Locate and identify every blood parasite.
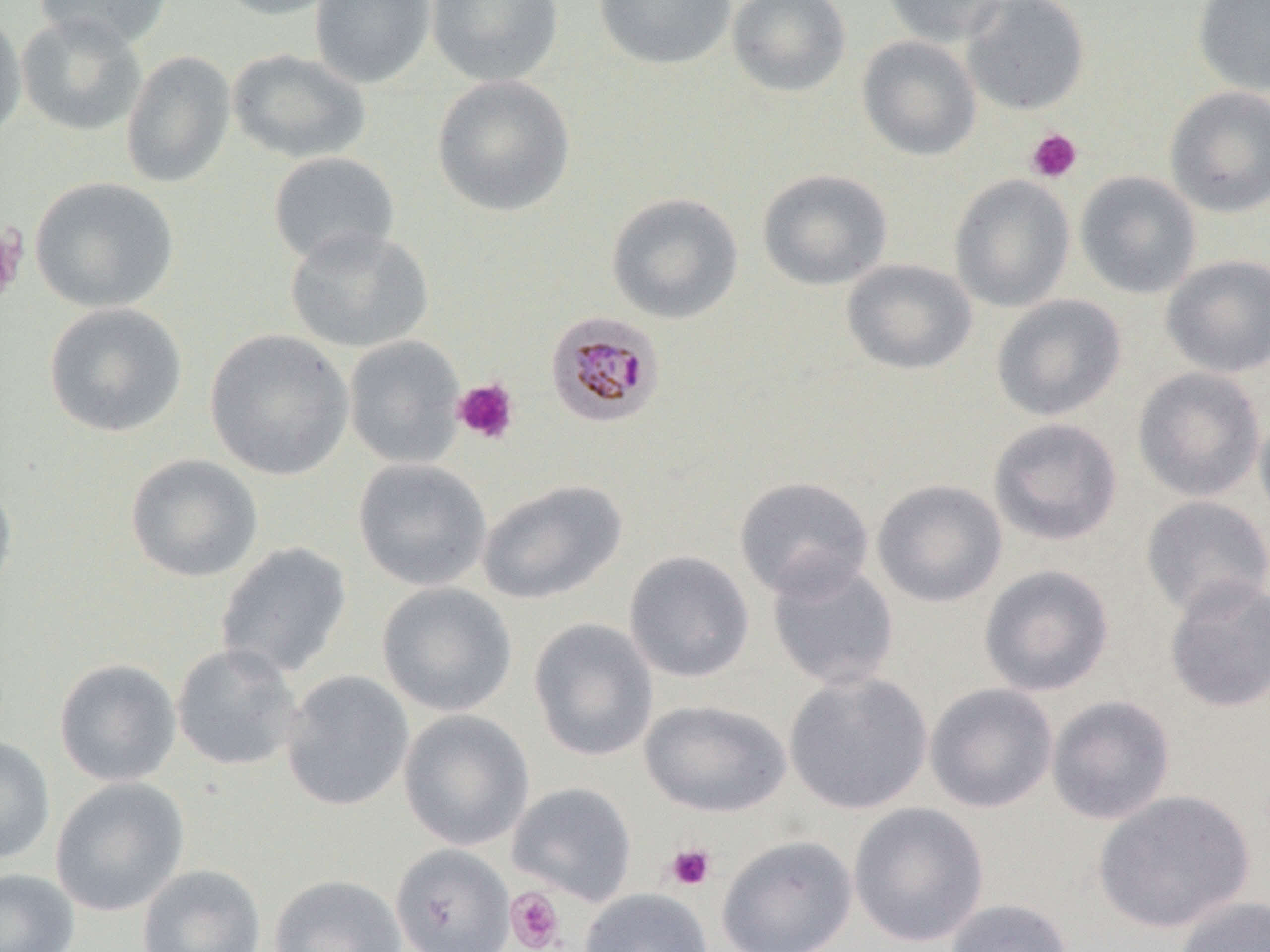

Approximate bounding boxes as (x1, y1, x2, y2) in pixels.
Plasmodium malariae-infected red blood cells: (545, 312, 665, 428).
No Plasmodium falciparum, Plasmodium ovale, Plasmodium vivax, Babesia divergens, or Trypanosoma brucei observed.

Summary:
  - Uninfected red blood cell locations: (33, 0, 174, 51), (210, 0, 345, 20), (310, 0, 436, 88), (426, 0, 564, 88), (593, 0, 737, 71), (727, 0, 852, 97), (881, 0, 1010, 47), (961, 0, 1091, 116), (1191, 0, 1270, 96), (0, 9, 27, 144), (16, 13, 147, 137), (857, 35, 982, 160), (227, 48, 371, 165), (120, 49, 236, 189), (431, 74, 575, 218), (1164, 86, 1270, 218), (268, 151, 400, 268), (757, 169, 893, 291), (1075, 171, 1201, 299), (949, 175, 1075, 312), (29, 177, 179, 314), (606, 192, 744, 324), (284, 226, 432, 353), (1161, 254, 1270, 378), (841, 259, 977, 376), (991, 294, 1126, 422), (43, 302, 187, 438), (204, 328, 354, 481), (343, 335, 466, 469), (1131, 366, 1266, 502), (1254, 406, 1270, 531), (988, 417, 1123, 546), (124, 453, 263, 583), (352, 458, 492, 591), (0, 476, 18, 602), (733, 476, 875, 601), (477, 479, 626, 605), (871, 479, 1008, 608), (1140, 495, 1270, 620), (215, 542, 352, 680), (623, 550, 755, 683), (766, 558, 900, 690), (978, 564, 1115, 697), (1164, 577, 1270, 713), (376, 581, 518, 716), (528, 617, 659, 761), (171, 642, 304, 772), (54, 658, 182, 787), (280, 670, 414, 812), (783, 671, 933, 815), (924, 682, 1058, 813), (1045, 694, 1176, 825), (639, 699, 792, 818), (398, 709, 534, 851), (0, 736, 55, 864), (49, 777, 189, 917), (507, 782, 637, 905), (1092, 789, 1256, 934), (847, 802, 990, 948), (716, 835, 858, 952), (390, 843, 515, 952), (136, 863, 266, 952), (0, 868, 80, 952), (268, 873, 407, 952), (579, 889, 713, 952), (1173, 895, 1270, 952), (944, 898, 1075, 952)
  - Platelet locations: (1026, 128, 1082, 183), (0, 225, 26, 307), (452, 378, 520, 445), (665, 843, 716, 891), (505, 887, 565, 952)
  - Slide-level diagnosis: Plasmodium malariae
  - Modality: light microscopy
  - Stain: May-Grünwald-Giemsa
  - Image size: 1270×952 pixels
  - Preparation: thin blood smear
  - Field of view: one of a larger specimen
  - Magnification: 1000x